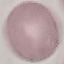

Result: no malaria parasites detected. Giemsa stain. Automatically extracted cell patch, resized to 64 × 64 pixels. Acquired by smartphone through the microscope eyepiece. Thin smear of blood.